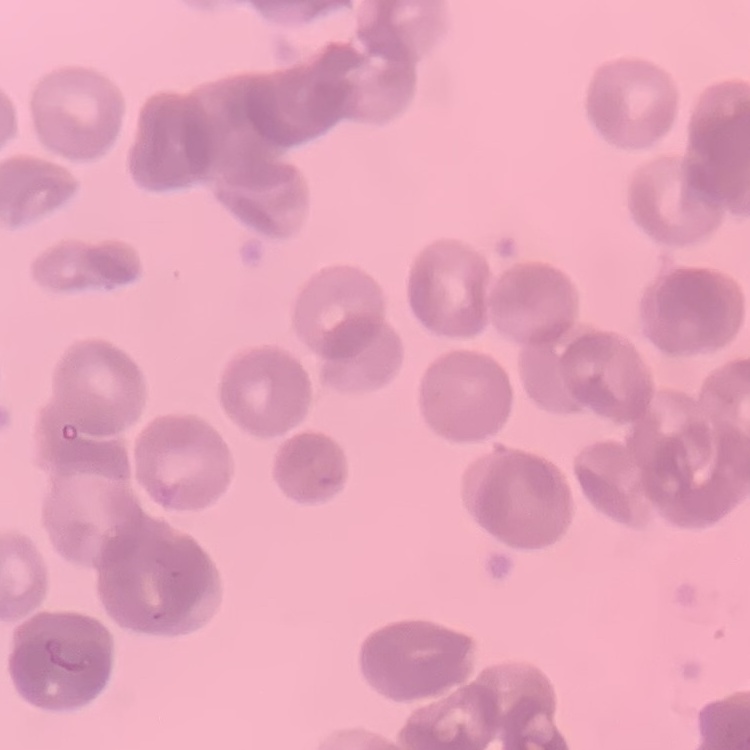
{
  "red_blood_cell_morphology": "rouleaux formation",
  "preparation": "thin blood film",
  "stain": "Field's or Giemsa",
  "image_type": "square crop of a larger photomicrograph"
}